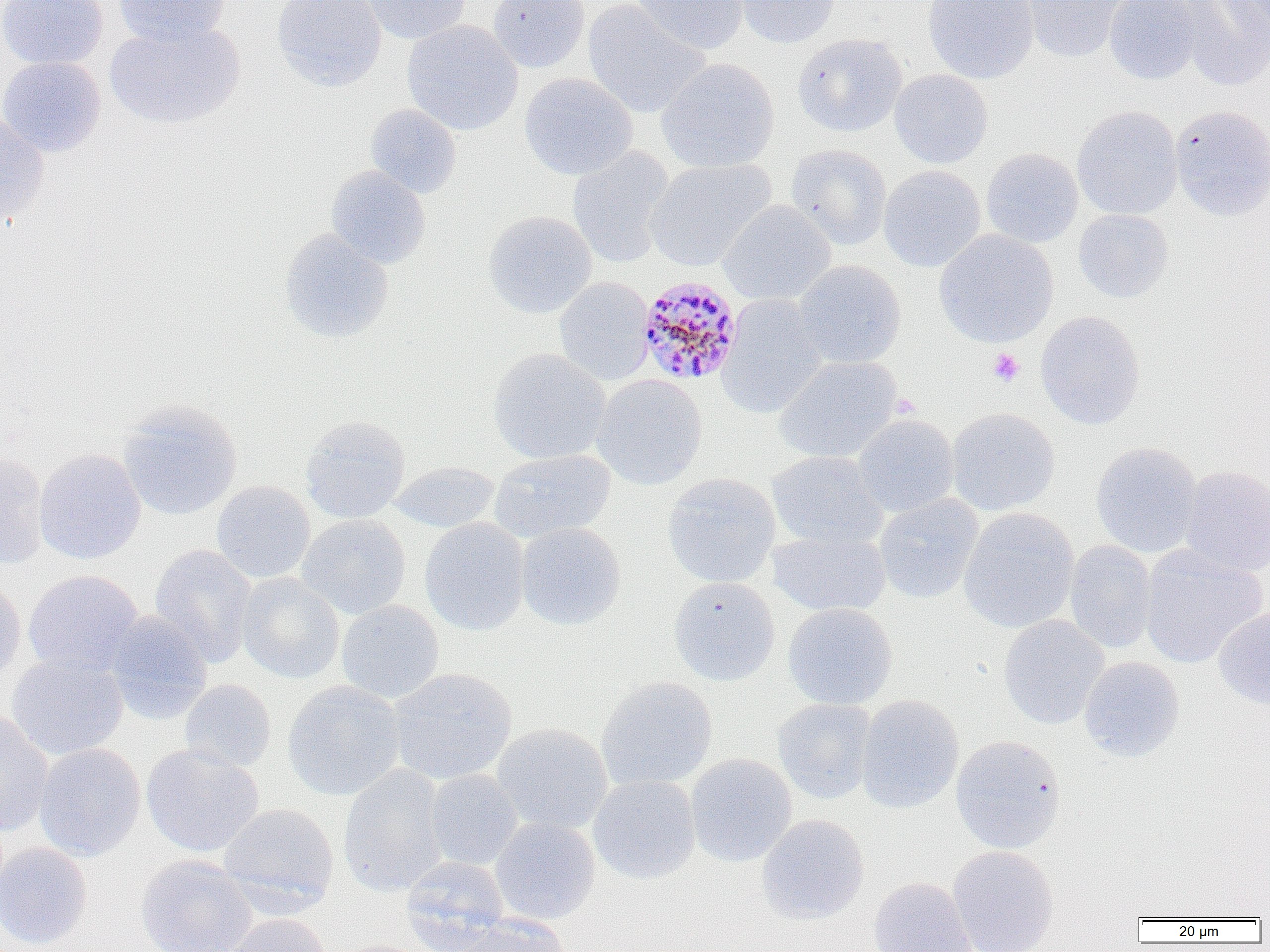
Summary:
  - Coordinate format: approximate bounding boxes as (x1,y1)-(x2,y2) corner pairs in pixels
  - Platelet locations: (987,347)-(1025,386), (890,392)-(922,418)
  - Plasmodium malariae-infected red blood cell locations: (637,273)-(743,385)
  - Uninfected red blood cell locations: (0,0)-(109,69), (113,0)-(230,48), (273,0)-(386,91), (361,0)-(471,44), (487,0)-(589,73), (633,0)-(749,55), (735,0)-(843,49), (923,0)-(1039,84), (1024,0)-(1129,62), (1103,0)-(1204,85), (1176,0)-(1270,91), (1223,0)-(1270,58), (583,1)-(709,118), (105,20)-(245,129), (402,20)-(523,136), (792,33)-(908,138), (0,56)-(106,157), (656,58)-(779,173), (889,69)-(993,168), (519,73)-(638,180), (365,104)-(462,198), (1169,104)-(1270,222), (1072,106)-(1183,220), (0,114)-(49,224), (786,144)-(891,250), (567,147)-(675,268), (981,147)-(1083,248), (645,158)-(776,271), (326,165)-(430,268), (878,165)-(986,272), (717,201)-(836,305), (1073,209)-(1173,303), (483,210)-(597,318), (279,228)-(394,343), (933,229)-(1059,347), (793,260)-(906,368), (554,277)-(655,385), (717,295)-(829,419), (1035,311)-(1145,430), (488,348)-(610,464), (774,356)-(902,463), (592,374)-(708,490), (118,399)-(242,521), (946,407)-(1059,516), (852,414)-(959,517), (300,415)-(411,523), (1090,442)-(1202,558), (34,448)-(146,565), (489,449)-(615,543), (767,451)-(888,550), (0,452)-(48,570), (389,461)-(500,533), (1179,464)-(1270,576), (661,473)-(781,587), (211,480)-(315,583), (874,494)-(983,604), (958,507)-(1079,633), (296,515)-(411,619), (420,517)-(530,635), (516,522)-(626,631), (768,527)-(890,617), (1064,540)-(1159,654), (149,544)-(257,668), (1139,545)-(1268,668), (23,569)-(144,677), (236,573)-(345,684), (0,576)-(26,686), (669,576)-(781,686), (336,600)-(444,703), (782,602)-(898,710), (1214,605)-(1270,711), (105,611)-(212,724), (998,615)-(1109,730), (6,653)-(128,760), (1078,656)-(1184,761), (388,667)-(517,784), (595,676)-(717,791), (179,679)-(276,773), (282,680)-(405,800), (855,695)-(964,814), (773,698)-(877,804), (0,709)-(53,837), (491,722)-(613,835), (950,734)-(1066,854), (34,743)-(146,861), (141,744)-(264,857), (685,753)-(797,867), (338,764)-(450,897), (424,769)-(523,870), (588,774)-(701,884), (218,803)-(339,912), (756,814)-(869,924), (489,817)-(600,925), (0,842)-(91,950), (947,845)-(1059,952), (135,854)-(257,952), (400,855)-(510,952), (868,876)-(977,952), (221,913)-(333,952), (450,914)-(571,952), (329,939)-(443,952)
  - Slide-level diagnosis: Plasmodium malariae
  - Field of view: single
  - Image size: 1270×952 pixels
  - Modality: light microscopy
  - Preparation: thin blood smear
  - Magnification: 1000x